Describe the morphology of the erythrocytes.
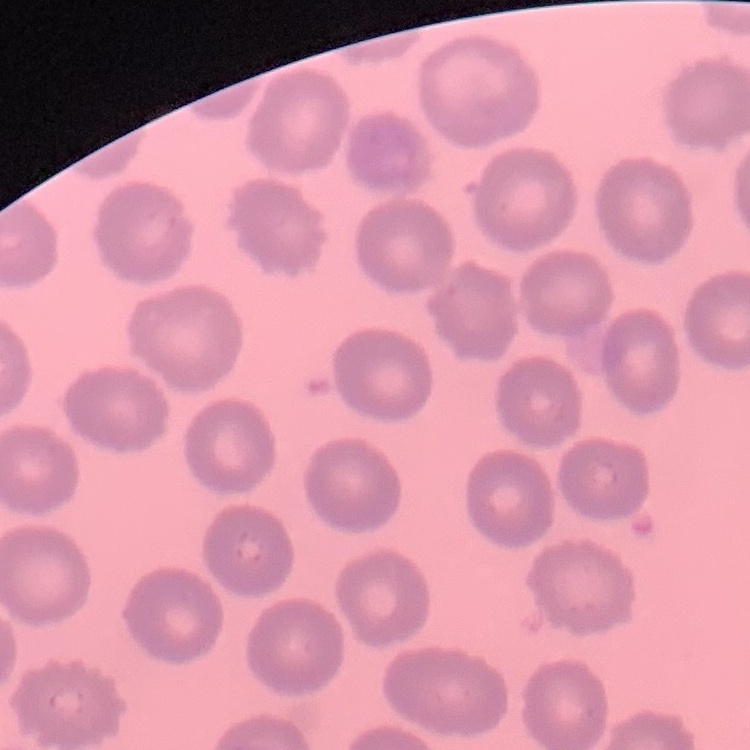

No rouleaux formation.

{
  "stain": "Field's or Giemsa",
  "image_type": "square crop of a larger photomicrograph",
  "preparation": "thin blood smear"
}